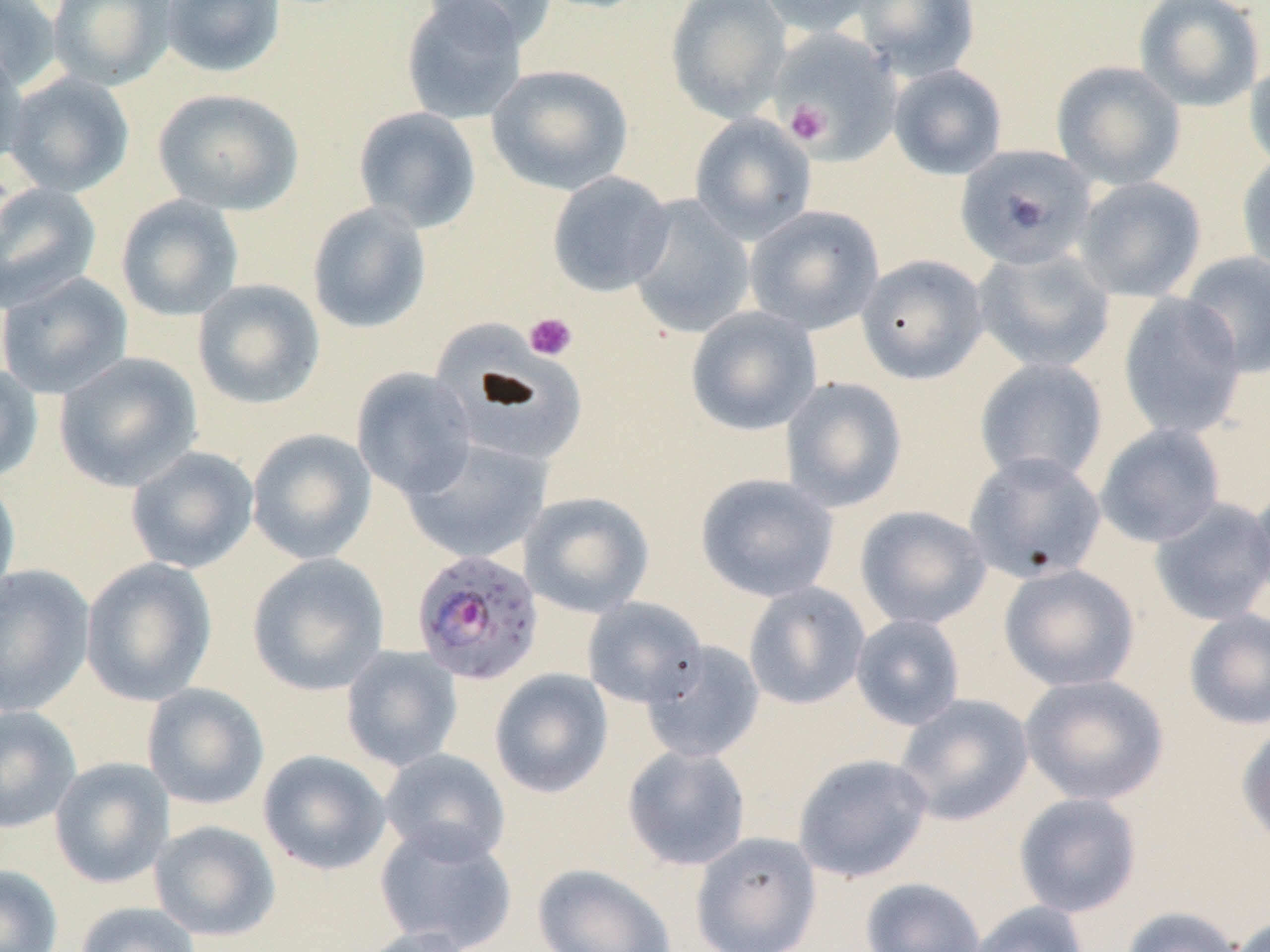

Summary:
  - Coordinate format: approximate bounding boxes as (x1,y1)-(x2,y2) corner pairs in pixels
  - White blood cell locations: (440,316)-(594,462)
  - Platelet locations: (777,75)-(859,152), (785,101)-(832,146), (523,312)-(578,362)
  - Plasmodium falciparum-infected red blood cell locations: (411,549)-(545,684)
  - Uninfected red blood cell locations: (0,0)-(62,93), (47,0)-(175,90), (159,0)-(286,78), (400,0)-(529,124), (421,0)-(559,49), (665,0)-(792,124), (755,0)-(884,36), (852,0)-(980,80), (1133,0)-(1265,112), (771,28)-(902,163), (0,46)-(29,173), (1244,53)-(1270,177), (1051,61)-(1186,191), (486,64)-(634,196), (888,64)-(1007,180), (3,72)-(134,197), (152,87)-(304,215), (353,106)-(482,233), (689,113)-(817,244), (955,143)-(1097,270), (1236,151)-(1270,276), (547,171)-(675,297), (1073,176)-(1207,302), (0,182)-(102,313), (115,194)-(244,322), (627,195)-(755,338), (306,201)-(432,334), (744,205)-(884,335), (972,248)-(1116,375), (1179,251)-(1270,379), (856,254)-(989,385), (0,271)-(134,398), (192,279)-(325,410), (1117,293)-(1247,440), (686,305)-(822,436), (54,351)-(203,491), (973,357)-(1109,486), (0,363)-(44,483), (351,367)-(477,500), (780,376)-(908,513), (1094,423)-(1226,547), (247,428)-(377,564), (403,437)-(551,563), (125,446)-(259,573), (963,451)-(1107,584), (695,472)-(839,602), (0,475)-(20,603), (1250,477)-(1270,603), (519,491)-(655,618), (1149,497)-(1270,626), (854,505)-(992,629), (247,553)-(390,696), (80,557)-(217,706), (998,564)-(1140,692), (0,565)-(95,716), (743,581)-(870,710), (583,597)-(706,708), (1183,609)-(1270,730), (849,614)-(966,730), (640,641)-(765,763), (341,645)-(463,772), (489,668)-(614,798), (1019,673)-(1169,807), (142,682)-(269,810), (893,693)-(1034,826), (0,706)-(81,833), (1236,721)-(1270,849), (621,744)-(751,871), (379,748)-(511,864), (258,749)-(391,875), (792,753)-(934,883), (49,757)-(174,888), (1013,792)-(1142,917), (149,819)-(281,941), (374,824)-(516,951), (689,831)-(822,952), (532,863)-(677,952), (0,864)-(62,952), (860,877)-(985,952), (966,901)-(1089,952), (75,902)-(202,952), (1118,905)-(1245,952), (1227,915)-(1270,952), (352,926)-(477,952)
  - Slide-level diagnosis: Plasmodium falciparum
  - Magnification: 1000x
  - Image size: 1270×952 pixels
  - Modality: light microscopy
  - Field of view: single
  - Preparation: thin blood smear
  - Stain: May-Grünwald-Giemsa